Assess this cell for malaria.
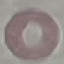
It is uninfected.

stain = Giemsa
preparation = thin blood film
image type = automatically extracted cell patch, resized to 64 × 64 pixels
capture = smartphone camera at the microscope eyepiece